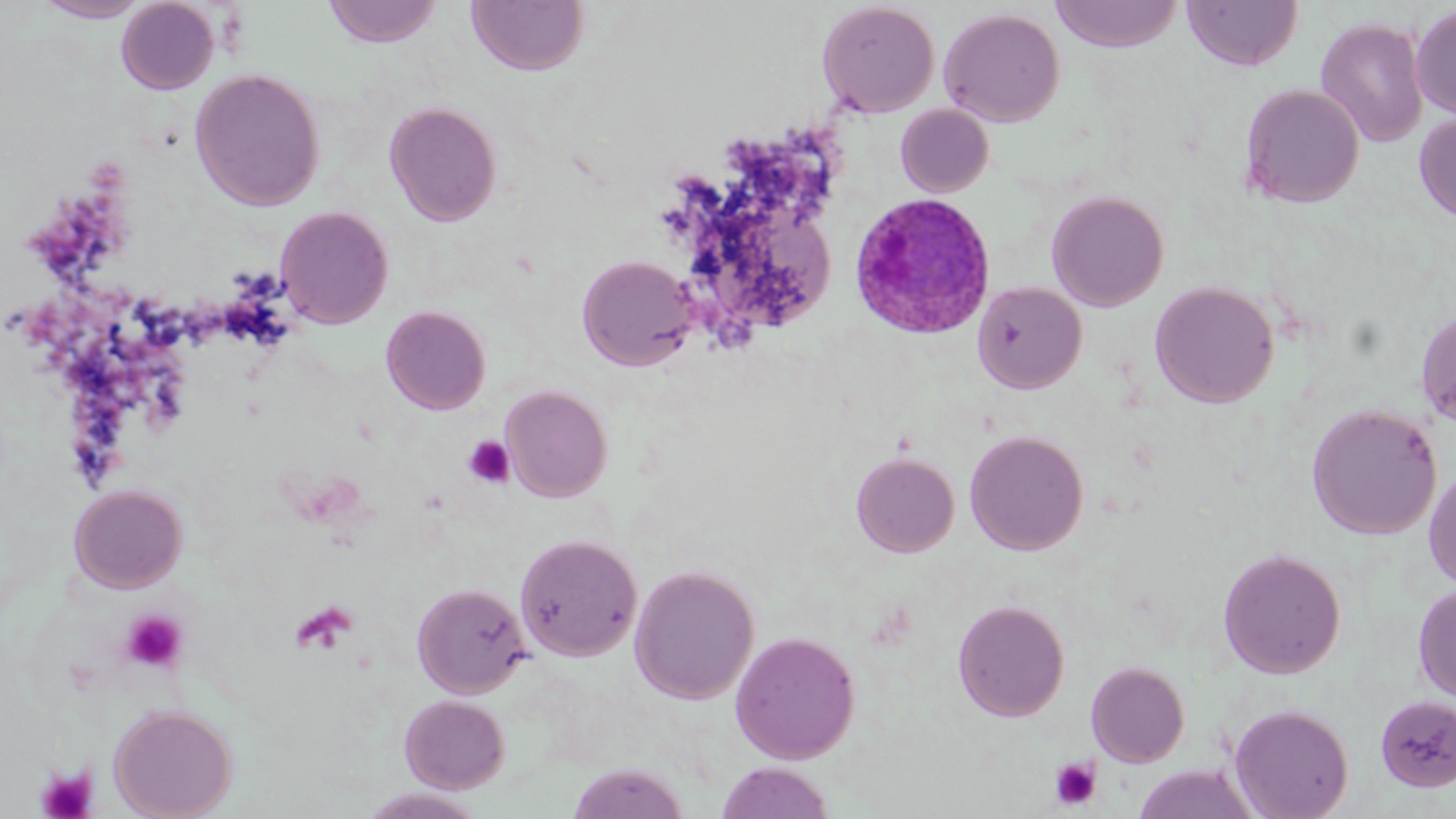

Plasmodium ovale-infected red blood cell locations = approximate bounding boxes as named x1/y1/x2/y2 corners in pixels: (x1=849, y1=192, x2=997, y2=340)
slide-level diagnosis = Plasmodium ovale
field of view = one of a larger specimen
uninfected red blood cell locations = approximate bounding boxes as named x1/y1/x2/y2 corners in pixels: (x1=34, y1=0, x2=150, y2=22), (x1=116, y1=0, x2=219, y2=94), (x1=322, y1=0, x2=443, y2=47), (x1=1182, y1=0, x2=1303, y2=71), (x1=467, y1=1, x2=589, y2=76), (x1=816, y1=1, x2=940, y2=117), (x1=1050, y1=1, x2=1183, y2=51), (x1=1411, y1=4, x2=1456, y2=119), (x1=939, y1=7, x2=1065, y2=127), (x1=1315, y1=17, x2=1429, y2=148), (x1=1261, y1=39, x2=1411, y2=171), (x1=189, y1=67, x2=326, y2=211), (x1=1240, y1=84, x2=1365, y2=208), (x1=384, y1=101, x2=502, y2=226), (x1=895, y1=104, x2=994, y2=197), (x1=1414, y1=111, x2=1456, y2=224), (x1=1046, y1=189, x2=1169, y2=311), (x1=275, y1=206, x2=394, y2=328), (x1=577, y1=254, x2=700, y2=371), (x1=972, y1=281, x2=1087, y2=394), (x1=1150, y1=281, x2=1279, y2=408), (x1=381, y1=305, x2=491, y2=414), (x1=1416, y1=306, x2=1456, y2=427), (x1=500, y1=385, x2=613, y2=502), (x1=1306, y1=403, x2=1442, y2=540), (x1=964, y1=429, x2=1088, y2=555), (x1=850, y1=451, x2=960, y2=557), (x1=1424, y1=465, x2=1456, y2=591), (x1=68, y1=484, x2=187, y2=593), (x1=514, y1=533, x2=642, y2=662), (x1=1218, y1=547, x2=1346, y2=678), (x1=629, y1=564, x2=759, y2=704), (x1=412, y1=582, x2=531, y2=699), (x1=1413, y1=584, x2=1456, y2=703), (x1=952, y1=599, x2=1070, y2=722), (x1=730, y1=630, x2=861, y2=764), (x1=1086, y1=661, x2=1190, y2=767), (x1=399, y1=695, x2=510, y2=793), (x1=1374, y1=695, x2=1456, y2=792), (x1=1230, y1=703, x2=1354, y2=819), (x1=109, y1=704, x2=237, y2=819), (x1=714, y1=761, x2=837, y2=819), (x1=566, y1=763, x2=690, y2=819), (x1=1131, y1=764, x2=1262, y2=819), (x1=358, y1=788, x2=488, y2=819)
image size = 1456×819 pixels
platelet locations = approximate bounding boxes as named x1/y1/x2/y2 corners in pixels: (x1=463, y1=435, x2=516, y2=489), (x1=292, y1=601, x2=359, y2=655), (x1=119, y1=609, x2=190, y2=674), (x1=1048, y1=756, x2=1103, y2=811), (x1=35, y1=764, x2=97, y2=819)
stain = May-Grünwald-Giemsa
preparation = thin blood smear
magnification = 1000x
modality = light microscopy